Locate every Plasmodium parasite.
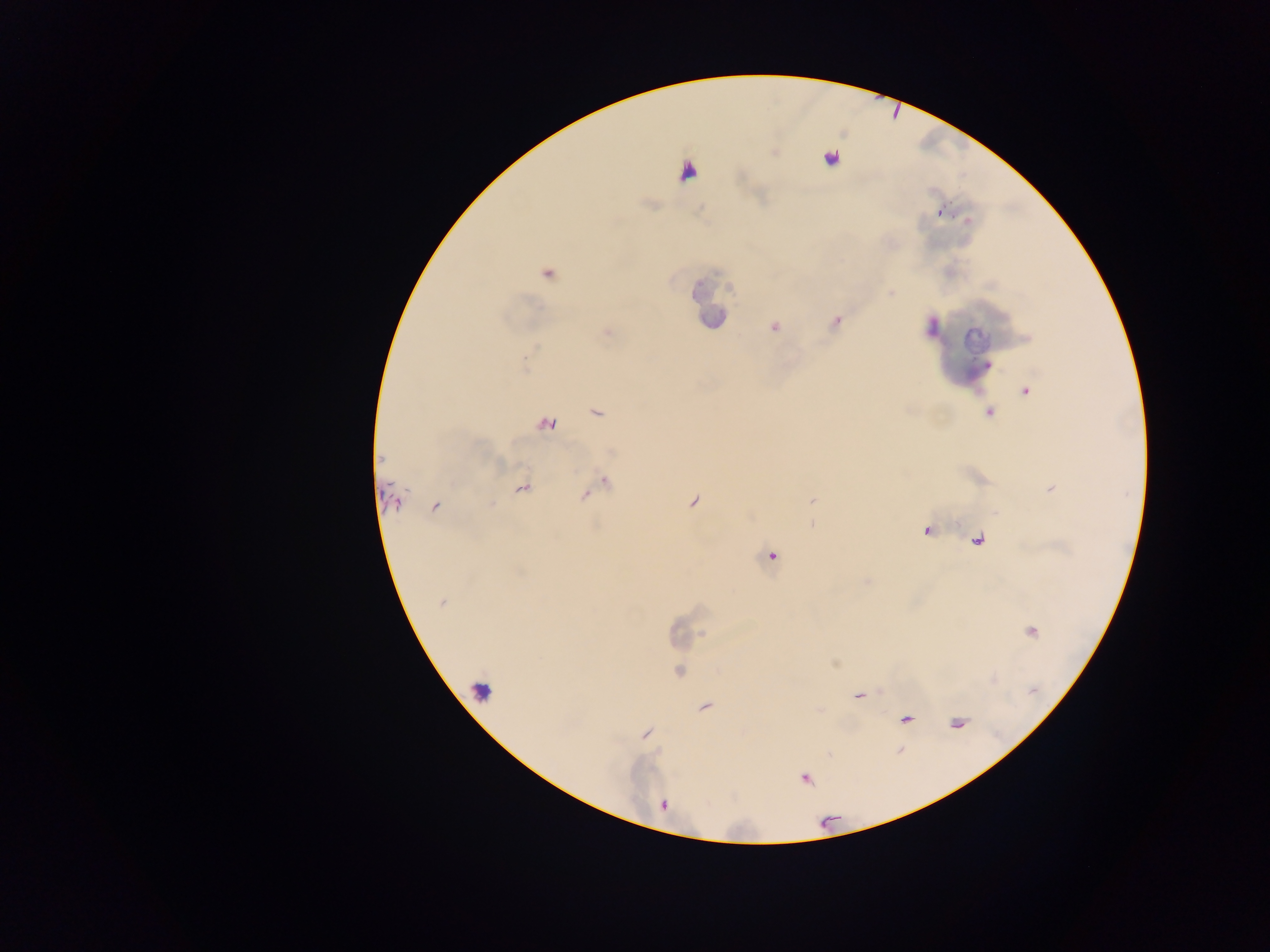
Approximate centers as x y in pixels.
Plasmodium parasites: 830 158; 940 212; 547 274; 891 293; 774 327; 1027 391; 597 413; 989 413; 547 423; 381 460; 605 482; 522 488; 394 501; 435 507; 979 536; 772 556; 441 602; 679 672; 705 706; 906 719; 960 722; 805 779; 664 805.

{
  "image_size": "1270×952 pixels",
  "field_of_view": "single",
  "leukocyte_locations": "approximate centers as x y in pixels: 689 166; 481 690",
  "country": "Ghana",
  "capture": "mobile-phone photograph through a microscope",
  "preparation": "thick blood film"
}